Assess this cell for malaria.
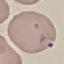
It is parasitized.

Summary:
  - Capture: smartphone camera at the microscope eyepiece
  - Image type: cell patch, automatically extracted from a larger field of view and resized to 64 × 64 pixels
  - Preparation: thin smear
  - Stain: Giemsa